Identify the parasite.
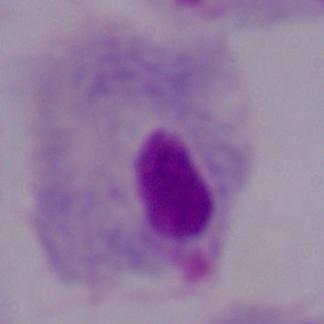

A trichomonad.

Summary:
  - Modality: micrograph
  - Magnification: 1000x